Comment on the morphology of the red blood cells.
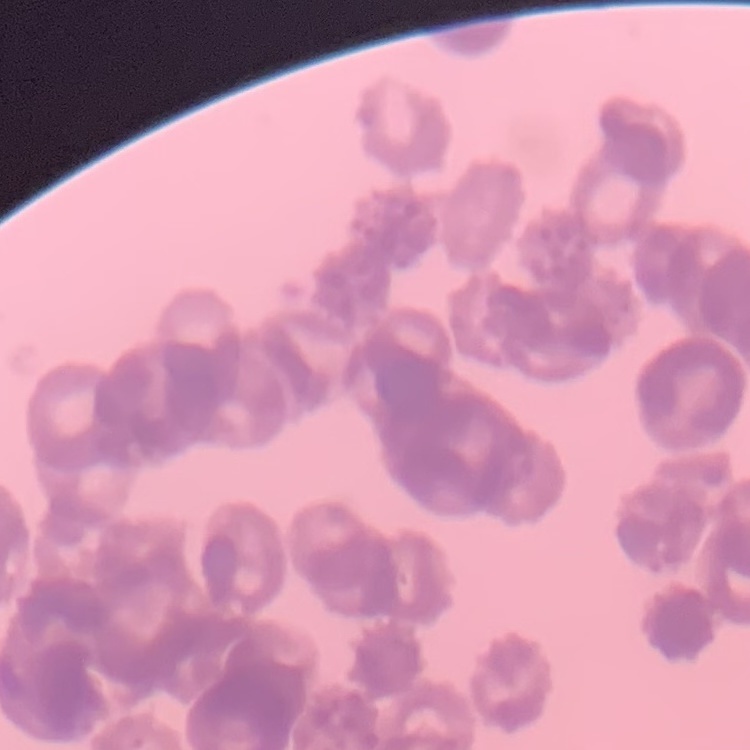

Rouleaux formation.

Thin blood film. Stained with either Field's or Giemsa. One tile cut from a larger photomicrograph.